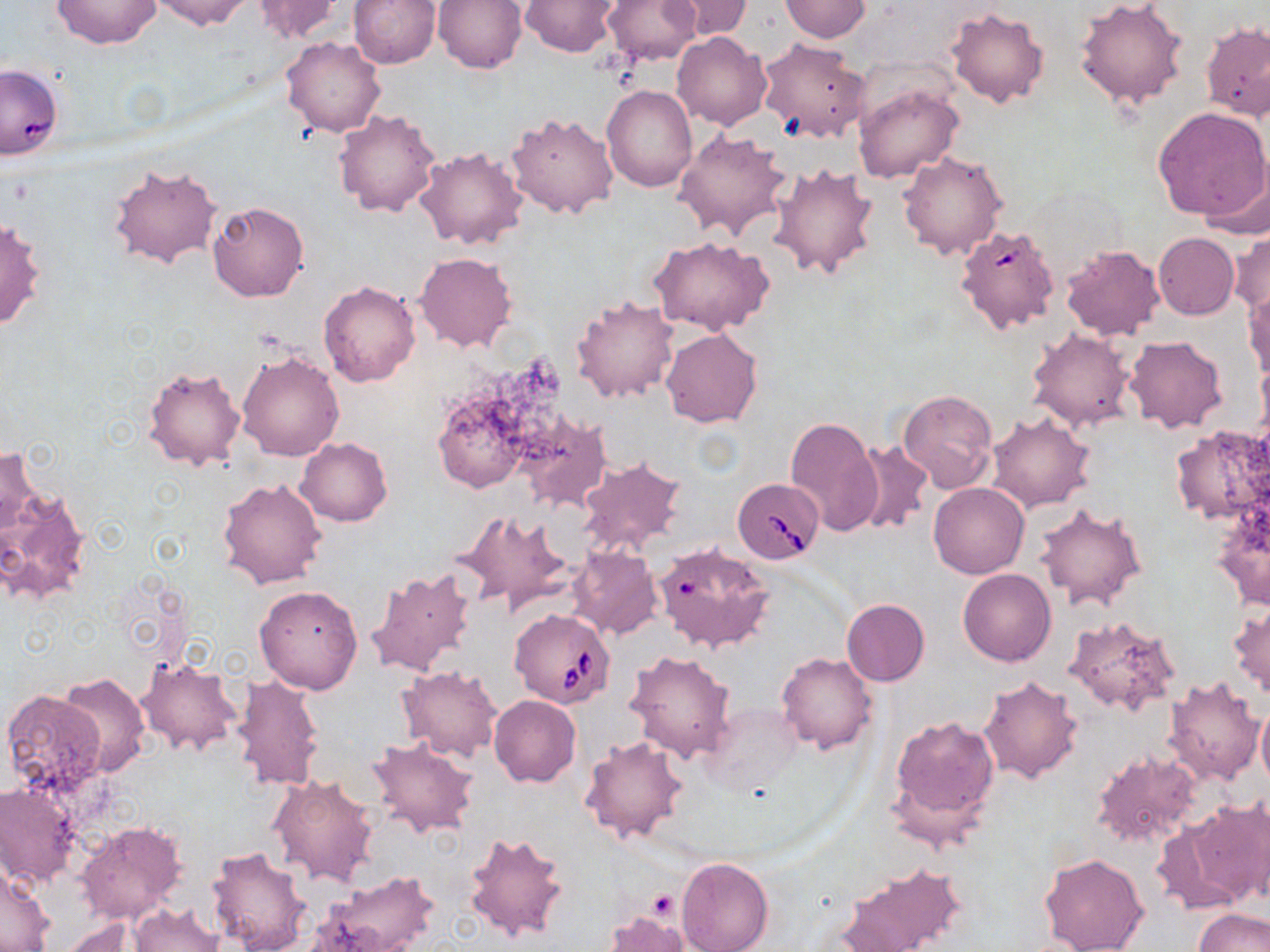
{
  "slide_level_diagnosis": "Babesia divergens",
  "uninfected_red_blood_cell_locations": "approximate bounding boxes as [x1, y1, x2, y2] in pixels: [51, 0, 162, 49], [150, 0, 253, 31], [251, 0, 346, 43], [435, 0, 527, 73], [520, 0, 620, 57], [603, 0, 702, 65], [665, 0, 753, 40], [1075, 0, 1189, 109], [346, 1, 440, 69], [780, 1, 871, 41], [945, 7, 1050, 109], [1202, 20, 1269, 123], [673, 32, 772, 131], [282, 37, 386, 137], [758, 39, 872, 142], [0, 64, 62, 161], [854, 82, 964, 184], [601, 84, 696, 192], [1154, 105, 1270, 225], [334, 109, 441, 218], [505, 112, 619, 218], [673, 129, 793, 242], [414, 146, 528, 251], [897, 151, 1008, 260], [108, 161, 223, 270], [769, 163, 880, 279], [207, 202, 309, 301], [1, 215, 47, 332], [955, 223, 1062, 335], [1230, 227, 1269, 317], [1153, 233, 1240, 319], [648, 236, 774, 335], [1060, 245, 1165, 342], [415, 252, 516, 352], [319, 280, 421, 387], [1244, 288, 1270, 382], [571, 294, 680, 403], [1026, 327, 1136, 432], [660, 328, 762, 427], [1124, 335, 1227, 434], [237, 348, 345, 461], [143, 364, 247, 473], [429, 364, 562, 496], [897, 389, 998, 495], [516, 411, 611, 512], [986, 411, 1094, 512], [785, 416, 881, 537], [1169, 424, 1270, 528], [296, 437, 392, 526], [853, 440, 932, 538], [1, 444, 39, 543], [576, 457, 685, 557], [218, 477, 327, 589], [928, 482, 1029, 578], [0, 483, 90, 605], [1210, 500, 1270, 612], [1034, 502, 1148, 612], [452, 509, 574, 618], [654, 543, 776, 653], [567, 547, 661, 641], [367, 566, 478, 678], [957, 568, 1056, 666], [254, 584, 365, 694], [841, 599, 929, 686], [1228, 603, 1270, 699], [1063, 616, 1181, 714], [625, 650, 736, 763], [777, 651, 877, 754], [136, 657, 240, 758], [398, 665, 503, 760], [58, 674, 149, 777], [232, 674, 323, 792], [978, 674, 1084, 784], [1163, 674, 1267, 785], [2, 689, 108, 799], [489, 695, 580, 787], [1256, 701, 1270, 796], [887, 713, 999, 836], [579, 734, 689, 845], [366, 737, 477, 839], [1091, 750, 1205, 852], [267, 773, 380, 887], [0, 779, 81, 890], [1181, 799, 1269, 906], [74, 820, 188, 924], [464, 831, 571, 944], [207, 846, 314, 952], [1038, 852, 1149, 952], [676, 857, 772, 952], [840, 863, 965, 951], [1, 866, 56, 951], [311, 872, 440, 952], [128, 903, 227, 952], [1195, 908, 1269, 952], [606, 910, 689, 952], [59, 917, 154, 951]",
  "platelet_locations": "approximate bounding boxes as [x1, y1, x2, y2] in pixels: [646, 891, 679, 920]",
  "babesia_divergens_infected_red_blood_cell_locations": "approximate bounding boxes as [x1, y1, x2, y2] in pixels: [731, 476, 823, 563], [509, 610, 616, 708]",
  "field_of_view": "single",
  "stain": "May-Grünwald-Giemsa",
  "preparation": "thin blood film",
  "magnification": "1000x",
  "modality": "optical microscopy",
  "image_size": "1270×952 pixels"
}